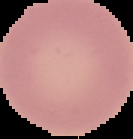
Summary:
  - Preparation: thin blood smear
  - Image size: 133×139 pixels
  - Malaria status: uninfected
  - Image type: cell region segmented out of the field of view; surrounding area masked to black